Locate and identify every blood parasite.
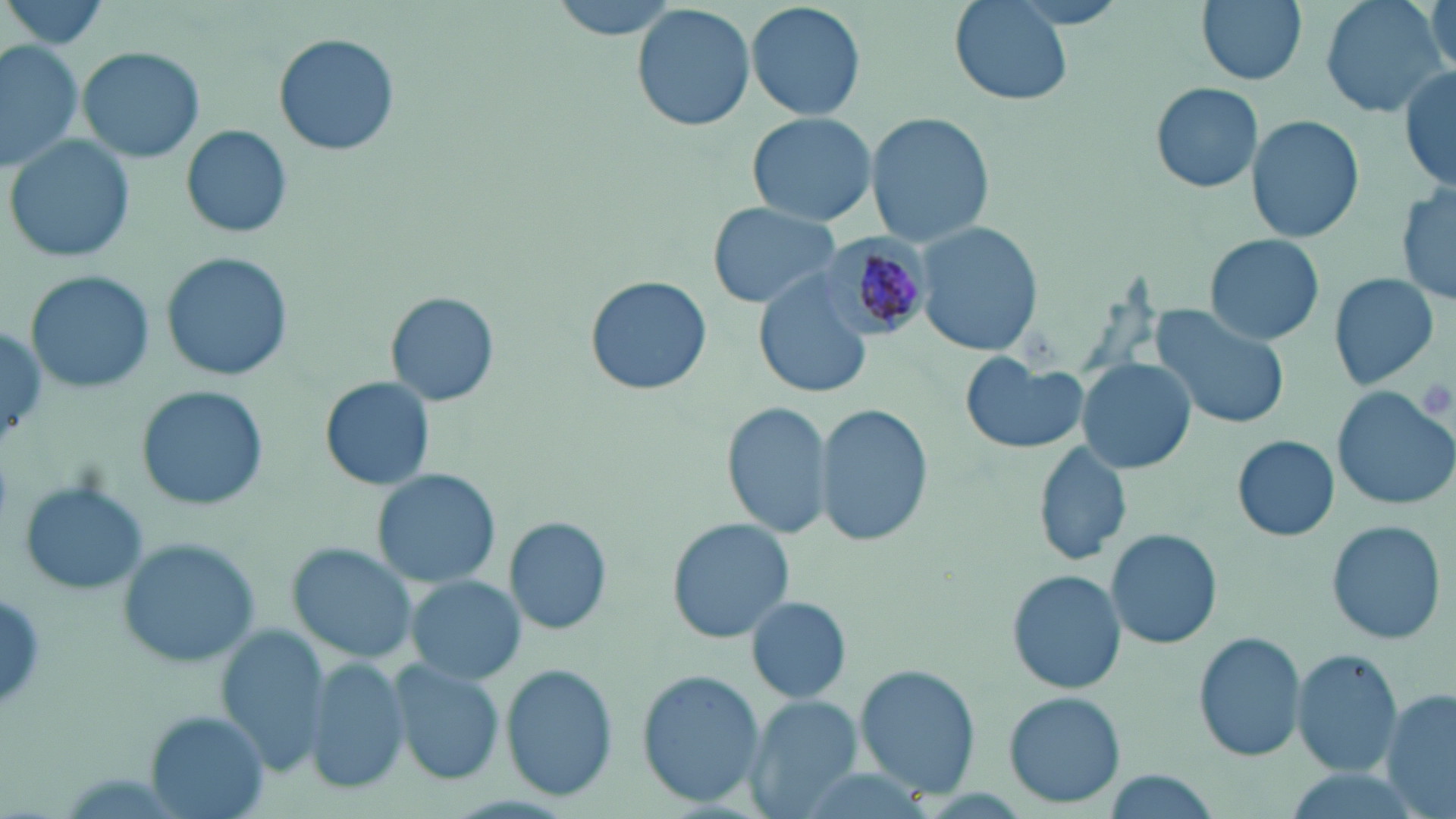
Approximate bounding boxes as [x1, y1, x2, y2] in pixels.
Plasmodium malariae-infected red blood cells: [819, 235, 933, 338].
No Plasmodium falciparum, Plasmodium ovale, Plasmodium vivax, Babesia divergens, or Trypanosoma brucei observed.

Summary:
  - Uninfected red blood cell locations: [1, 0, 113, 54], [547, 0, 683, 41], [745, 0, 867, 122], [1196, 0, 1308, 86], [1316, 0, 1448, 120], [1427, 0, 1455, 77], [950, 1, 1072, 107], [632, 3, 757, 133], [273, 32, 400, 158], [0, 38, 83, 174], [79, 45, 204, 164], [1399, 63, 1456, 195], [1150, 81, 1263, 195], [745, 110, 880, 226], [865, 111, 995, 249], [1246, 114, 1363, 244], [181, 125, 295, 238], [4, 135, 136, 264], [1397, 179, 1454, 309], [706, 201, 841, 310], [913, 222, 1042, 357], [1205, 233, 1323, 345], [162, 253, 296, 381], [24, 270, 154, 395], [1327, 272, 1440, 390], [756, 274, 872, 399], [585, 276, 712, 396], [386, 292, 498, 406], [1149, 302, 1290, 430], [959, 354, 1088, 455], [1077, 358, 1196, 475], [323, 376, 434, 489], [139, 386, 268, 511], [1332, 387, 1456, 510], [722, 399, 833, 541], [814, 404, 934, 548], [1232, 435, 1340, 541], [1030, 440, 1133, 567], [372, 469, 500, 588], [20, 480, 151, 595], [503, 516, 612, 635], [663, 518, 797, 643], [1325, 520, 1447, 646], [1105, 529, 1222, 648], [119, 540, 262, 668], [290, 543, 423, 662], [1008, 571, 1125, 693], [407, 576, 524, 684], [746, 596, 852, 706], [216, 624, 331, 776], [1193, 631, 1307, 762], [1291, 648, 1403, 777], [302, 657, 407, 797], [393, 660, 506, 784], [501, 664, 618, 802], [854, 664, 982, 799], [637, 667, 765, 809], [1382, 690, 1456, 817], [1005, 693, 1125, 804], [747, 697, 864, 816], [147, 712, 265, 817]
  - Platelet locations: [1416, 375, 1453, 420]
  - Slide-level diagnosis: Plasmodium malariae
  - Modality: light microscopy
  - Field of view: single
  - Stain: May-Grünwald-Giemsa
  - Preparation: thin blood film
  - Image size: 1456×819 pixels
  - Magnification: 1000x